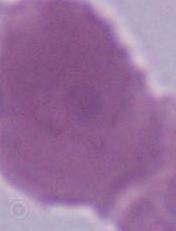
{
  "identification": "erythrocyte",
  "modality": "micrograph",
  "magnification": "1000x"
}